State which cell type is depicted.
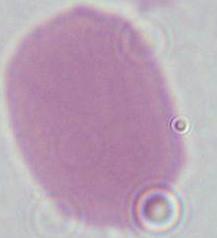
This is an erythrocyte.

modality = micrograph
magnification = 1000x